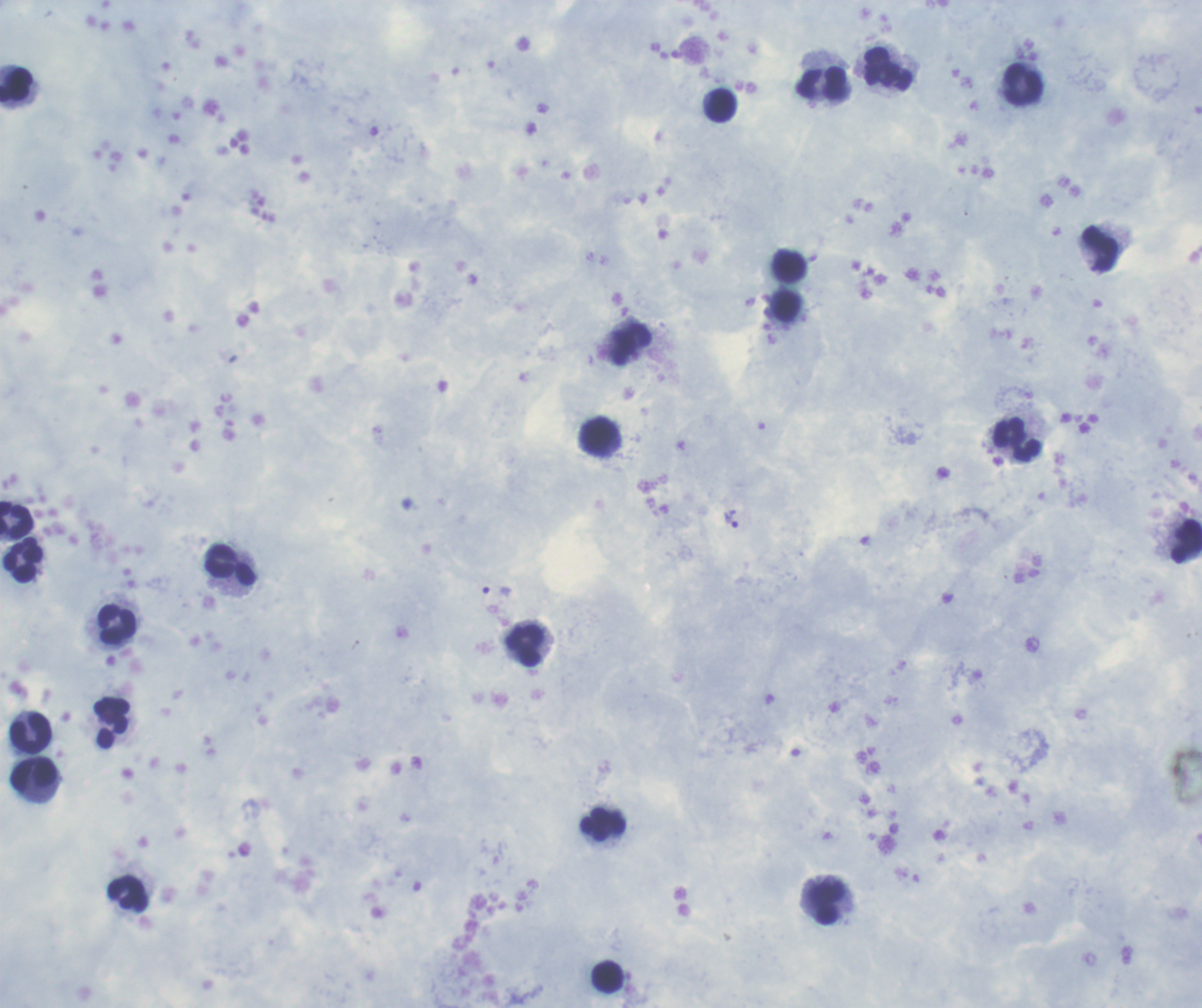
Approximate centers as (x, y) in pixels. Leukocyte locations: (888, 69), (821, 82), (1022, 84), (16, 86), (719, 104), (1100, 249), (786, 305), (630, 344), (599, 435), (1015, 439), (16, 520), (1186, 540), (23, 560), (230, 565), (117, 624), (524, 646), (111, 722), (30, 733), (34, 773), (603, 823), (128, 894), (827, 902), (607, 977). Trophozoite locations: (731, 519), (496, 590). Background quality: good. Image is 1202×1008 pixels. Coloration quality: good. Previously used in an actual diagnosis. Result: Plasmodium parasites identified. Romanowsky-stained preparation. Thick blood smear. Single field of view. 100x magnification.